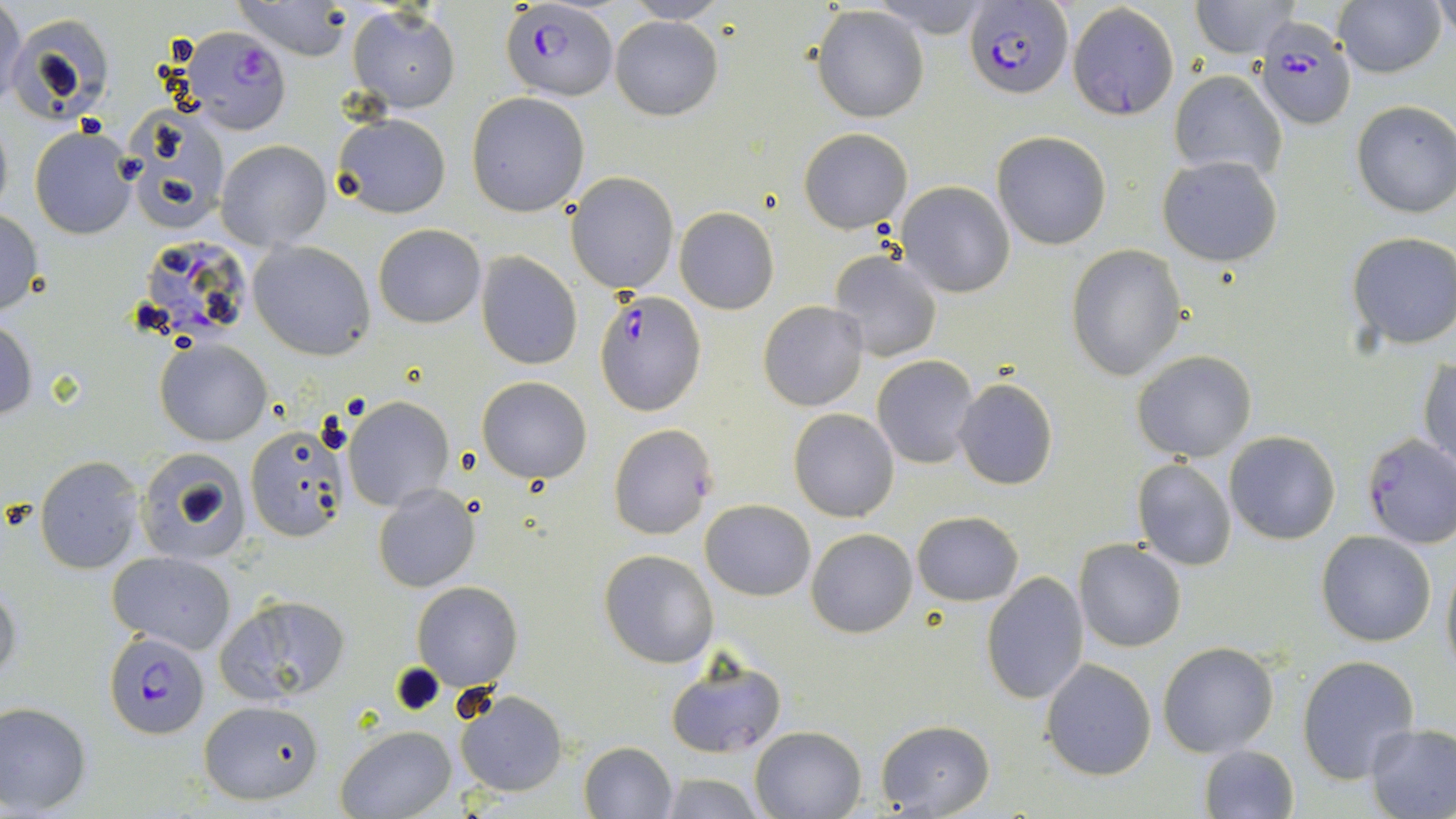

Plasmodium falciparum-infected red blood cell locations = approximate bounding boxes as named x1/y1/x2/y2 corners in pixels: (x1=499, y1=3, x2=618, y2=103), (x1=966, y1=3, x2=1073, y2=98), (x1=1253, y1=19, x2=1356, y2=129), (x1=180, y1=25, x2=292, y2=134), (x1=131, y1=233, x2=258, y2=349), (x1=593, y1=292, x2=707, y2=415), (x1=1361, y1=434, x2=1456, y2=549), (x1=103, y1=632, x2=208, y2=737)
slide-level diagnosis = Plasmodium falciparum
stain = May-Grünwald-Giemsa
modality = light microscopy
magnification = 1000x
preparation = thin blood smear
field of view = single
uninfected red blood cell locations = approximate bounding boxes as named x1/y1/x2/y2 corners in pixels: (x1=0, y1=0, x2=26, y2=113), (x1=622, y1=1, x2=730, y2=24), (x1=1067, y1=1, x2=1179, y2=122), (x1=1190, y1=1, x2=1301, y2=57), (x1=1336, y1=1, x2=1446, y2=79), (x1=234, y1=2, x2=353, y2=61), (x1=1433, y1=2, x2=1456, y2=46), (x1=347, y1=6, x2=461, y2=113), (x1=812, y1=6, x2=930, y2=123), (x1=6, y1=14, x2=114, y2=124), (x1=609, y1=15, x2=723, y2=120), (x1=1170, y1=70, x2=1288, y2=186), (x1=466, y1=93, x2=590, y2=216), (x1=1351, y1=100, x2=1456, y2=218), (x1=119, y1=104, x2=230, y2=232), (x1=331, y1=111, x2=452, y2=218), (x1=0, y1=112, x2=13, y2=223), (x1=29, y1=127, x2=138, y2=239), (x1=799, y1=127, x2=914, y2=233), (x1=992, y1=131, x2=1111, y2=249), (x1=216, y1=139, x2=332, y2=249), (x1=1158, y1=156, x2=1283, y2=268), (x1=567, y1=173, x2=679, y2=294), (x1=895, y1=180, x2=1016, y2=298), (x1=674, y1=207, x2=779, y2=314), (x1=0, y1=209, x2=45, y2=317), (x1=373, y1=223, x2=485, y2=328), (x1=1345, y1=233, x2=1456, y2=349), (x1=248, y1=240, x2=375, y2=359), (x1=1066, y1=243, x2=1185, y2=380), (x1=829, y1=250, x2=942, y2=362), (x1=475, y1=252, x2=584, y2=369), (x1=757, y1=301, x2=869, y2=412), (x1=0, y1=319, x2=37, y2=421), (x1=155, y1=338, x2=272, y2=446), (x1=1132, y1=350, x2=1256, y2=461), (x1=872, y1=355, x2=978, y2=468), (x1=1419, y1=359, x2=1455, y2=467), (x1=478, y1=376, x2=593, y2=483), (x1=953, y1=376, x2=1059, y2=491), (x1=343, y1=397, x2=454, y2=511), (x1=789, y1=409, x2=899, y2=523), (x1=608, y1=423, x2=717, y2=539), (x1=245, y1=427, x2=351, y2=542), (x1=1225, y1=432, x2=1341, y2=545), (x1=135, y1=447, x2=254, y2=564), (x1=35, y1=457, x2=144, y2=573), (x1=1130, y1=457, x2=1239, y2=572), (x1=372, y1=483, x2=480, y2=594), (x1=701, y1=500, x2=815, y2=600), (x1=911, y1=510, x2=1023, y2=606), (x1=807, y1=528, x2=917, y2=638), (x1=1317, y1=531, x2=1436, y2=646), (x1=1075, y1=539, x2=1186, y2=652), (x1=598, y1=549, x2=719, y2=668), (x1=106, y1=550, x2=237, y2=654), (x1=1440, y1=554, x2=1456, y2=674), (x1=981, y1=571, x2=1089, y2=705), (x1=0, y1=579, x2=21, y2=688), (x1=411, y1=582, x2=522, y2=688), (x1=213, y1=592, x2=349, y2=704), (x1=1157, y1=642, x2=1278, y2=757), (x1=663, y1=652, x2=786, y2=760), (x1=1297, y1=655, x2=1420, y2=785), (x1=1042, y1=659, x2=1155, y2=781), (x1=454, y1=687, x2=569, y2=798), (x1=198, y1=699, x2=327, y2=806), (x1=0, y1=701, x2=91, y2=815), (x1=875, y1=720, x2=993, y2=817), (x1=1363, y1=724, x2=1456, y2=819), (x1=750, y1=725, x2=867, y2=817), (x1=334, y1=726, x2=455, y2=819), (x1=577, y1=740, x2=677, y2=818), (x1=1197, y1=745, x2=1300, y2=819), (x1=656, y1=772, x2=767, y2=818)
image size = 1456×819 pixels